Assess this cell for malaria.
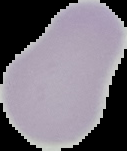
Uninfected.

Summary:
  - Image size: 127×151 pixels
  - Preparation: thin blood film
  - Image type: cell region segmented out of the field of view; surrounding area masked to black